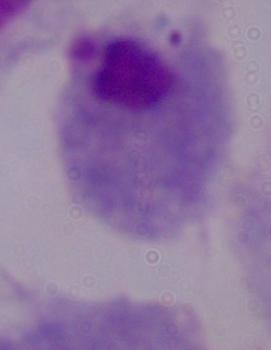
Micrograph. A trichomonad is shown. Captured at 1000x magnification.